Describe the morphology of the red blood cells.
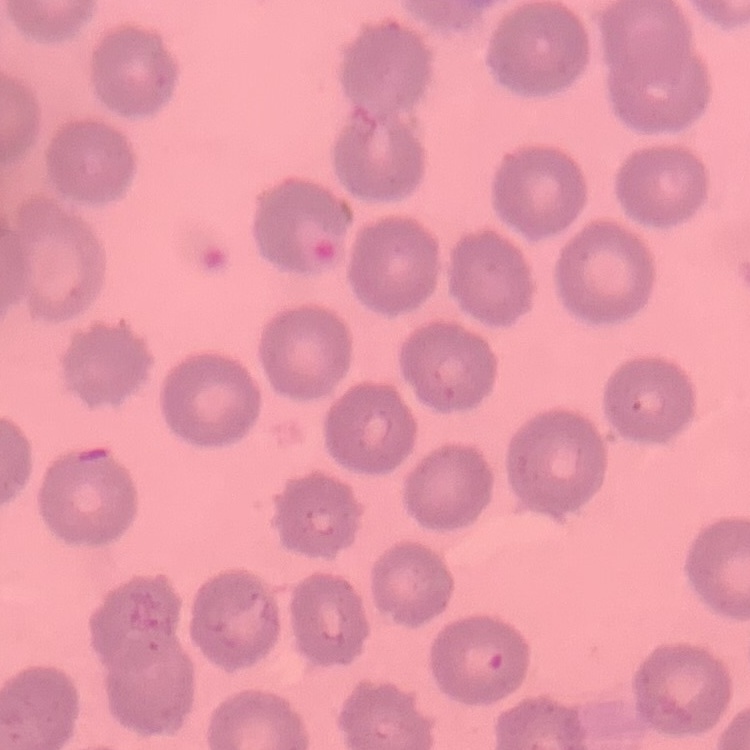

No rouleaux formation.

Summary:
  - Preparation: thin peripheral smear
  - Image type: square crop of a larger photomicrograph
  - Stain: Field's or Giemsa